State the blood parasite species.
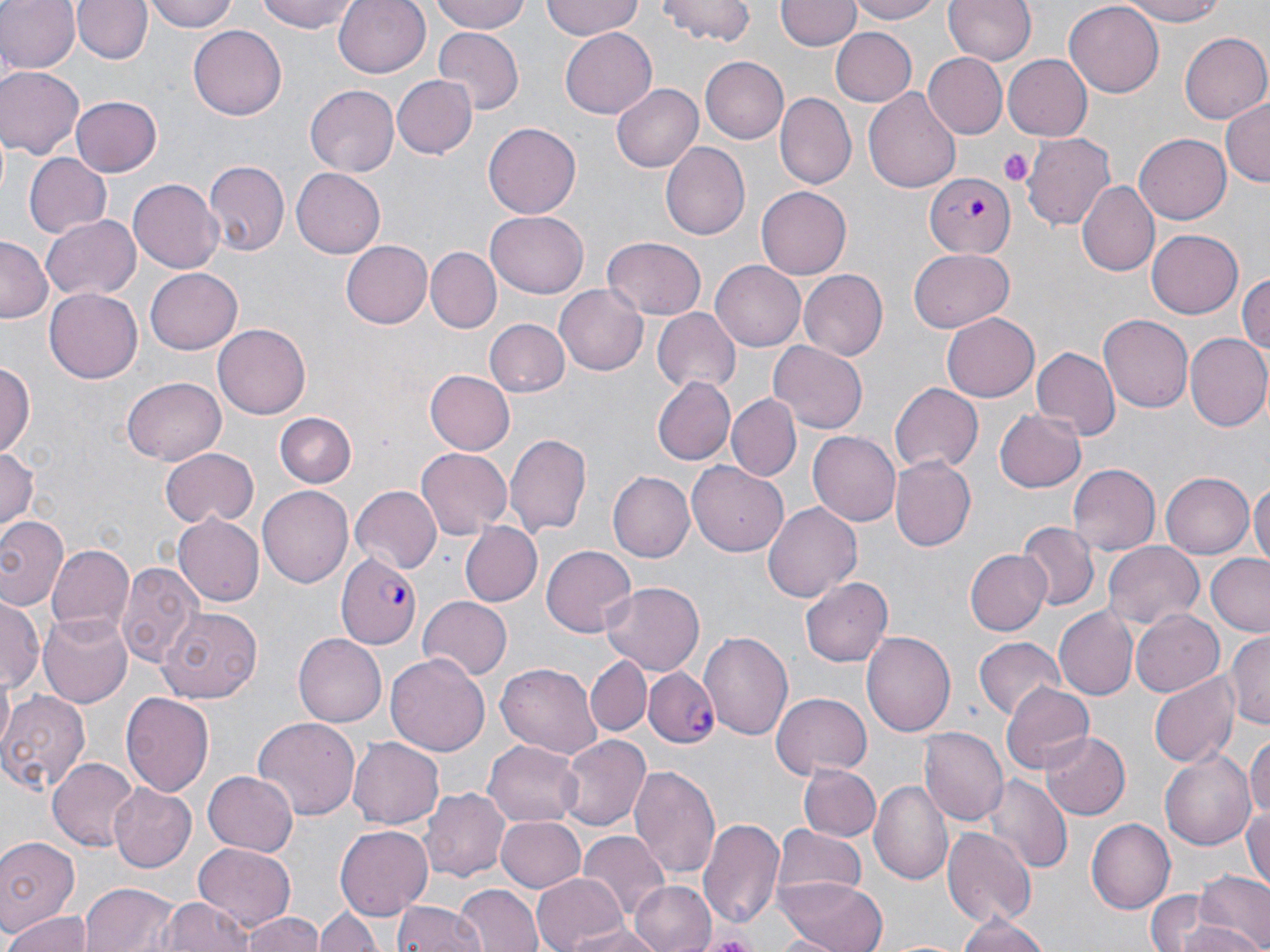
Plasmodium falciparum.

Summary:
  - Coordinate format: approximate bounding boxes as (x1, y1, x2, y2) in pixels
  - Plasmodium falciparum-infected red blood cell locations: (925, 174, 1014, 258), (337, 556, 422, 647), (645, 666, 718, 748)
  - Uninfected red blood cell locations: (0, 0, 78, 74), (73, 0, 150, 64), (145, 0, 239, 33), (258, 0, 358, 32), (332, 0, 430, 79), (429, 0, 534, 36), (543, 0, 645, 42), (657, 0, 756, 47), (776, 0, 859, 52), (846, 0, 947, 24), (943, 0, 1037, 64), (1115, 0, 1230, 26), (1063, 3, 1163, 99), (189, 24, 288, 119), (831, 26, 915, 107), (559, 28, 658, 118), (434, 29, 523, 112), (1180, 31, 1269, 123), (701, 54, 789, 144), (924, 54, 1006, 138), (1005, 54, 1092, 143), (0, 66, 83, 159), (392, 74, 476, 160), (613, 81, 703, 171), (305, 84, 400, 177), (863, 88, 961, 194), (776, 92, 856, 190), (70, 96, 162, 177), (1221, 96, 1270, 185), (484, 122, 580, 219), (1024, 133, 1116, 232), (1136, 133, 1230, 223), (660, 141, 750, 240), (23, 154, 112, 239), (203, 160, 290, 259), (291, 167, 386, 259), (129, 180, 223, 273), (1077, 181, 1160, 278), (755, 186, 851, 280), (487, 214, 587, 299), (42, 215, 141, 301), (1147, 229, 1244, 318), (601, 236, 707, 319), (0, 239, 50, 323), (341, 239, 433, 328), (908, 247, 1016, 331), (427, 248, 500, 332), (710, 262, 805, 351), (145, 267, 241, 354), (798, 269, 888, 361), (1237, 269, 1269, 364), (555, 283, 650, 375), (45, 289, 142, 383), (651, 308, 739, 393), (940, 313, 1040, 403), (1098, 315, 1193, 413), (485, 320, 570, 397), (214, 323, 311, 418), (1185, 332, 1270, 431), (769, 342, 867, 433), (1033, 346, 1119, 438), (0, 359, 35, 463), (423, 370, 514, 455), (123, 375, 228, 463), (650, 376, 735, 466), (890, 383, 982, 474), (728, 395, 802, 481), (995, 409, 1086, 492), (273, 413, 357, 489), (807, 429, 901, 526), (504, 431, 593, 540), (0, 445, 38, 534), (159, 447, 259, 528), (415, 447, 512, 538), (890, 455, 975, 553), (688, 461, 789, 556), (1069, 463, 1160, 555), (611, 470, 697, 561), (1162, 471, 1258, 559), (1250, 478, 1270, 569), (260, 485, 353, 588), (349, 485, 444, 574), (764, 503, 860, 600), (171, 512, 265, 605), (0, 514, 67, 612), (458, 520, 542, 608), (1017, 522, 1097, 612), (1101, 540, 1204, 631), (45, 541, 132, 632), (540, 544, 637, 638), (964, 549, 1052, 636), (1207, 554, 1270, 638), (115, 562, 200, 669), (801, 577, 893, 668), (600, 582, 705, 675), (418, 596, 512, 680), (1, 598, 41, 692), (159, 608, 263, 702), (1055, 608, 1135, 699), (1132, 610, 1222, 696), (40, 611, 132, 707), (862, 629, 956, 737), (699, 630, 793, 740), (1225, 630, 1270, 729), (293, 633, 386, 727), (973, 635, 1064, 721), (385, 651, 490, 757), (585, 655, 651, 736), (496, 662, 601, 764), (1149, 671, 1237, 770), (998, 681, 1096, 775), (0, 691, 89, 796), (120, 691, 215, 798), (772, 693, 872, 777), (253, 715, 361, 819), (918, 727, 1007, 825), (1041, 730, 1130, 821), (1246, 731, 1270, 824), (559, 733, 651, 833), (350, 736, 446, 829), (483, 739, 583, 825), (1161, 751, 1259, 848), (49, 758, 137, 852), (798, 762, 880, 841), (629, 763, 721, 882), (203, 771, 298, 855), (985, 775, 1070, 874), (870, 779, 953, 889), (107, 783, 197, 872), (422, 787, 510, 879), (1244, 806, 1270, 888), (494, 815, 586, 894), (698, 816, 784, 926), (1088, 819, 1176, 913), (335, 824, 434, 919), (771, 825, 867, 905), (943, 826, 1036, 926), (579, 829, 670, 920), (0, 837, 79, 934), (190, 843, 296, 928), (1193, 872, 1269, 952), (530, 873, 627, 952), (203, 877, 309, 952), (779, 878, 884, 952), (630, 880, 717, 952), (81, 883, 180, 952), (455, 884, 542, 952), (1141, 888, 1223, 952), (157, 895, 251, 951), (390, 899, 484, 952), (316, 902, 382, 952), (239, 910, 326, 952), (4, 911, 92, 952), (957, 914, 1050, 952), (563, 924, 668, 952), (697, 931, 759, 949)
  - Platelet locations: (997, 147, 1031, 186)
  - Modality: optical microscopy
  - Magnification: 1000x
  - Stain: May-Grünwald-Giemsa
  - Field of view: one of a larger specimen
  - Image size: 1270×952 pixels
  - Preparation: thin blood film